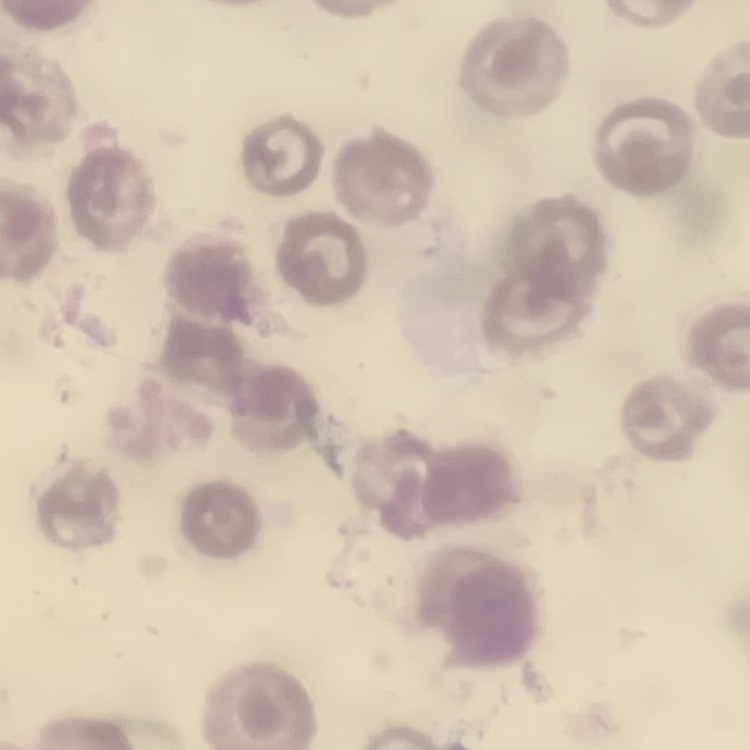
Summary:
  - Red blood cell morphology: no rouleaux formation
  - Image type: one tile cut from a larger photomicrograph
  - Preparation: thin peripheral smear
  - Stain: Field's or Giemsa